Give the position of every leukocyte visible.
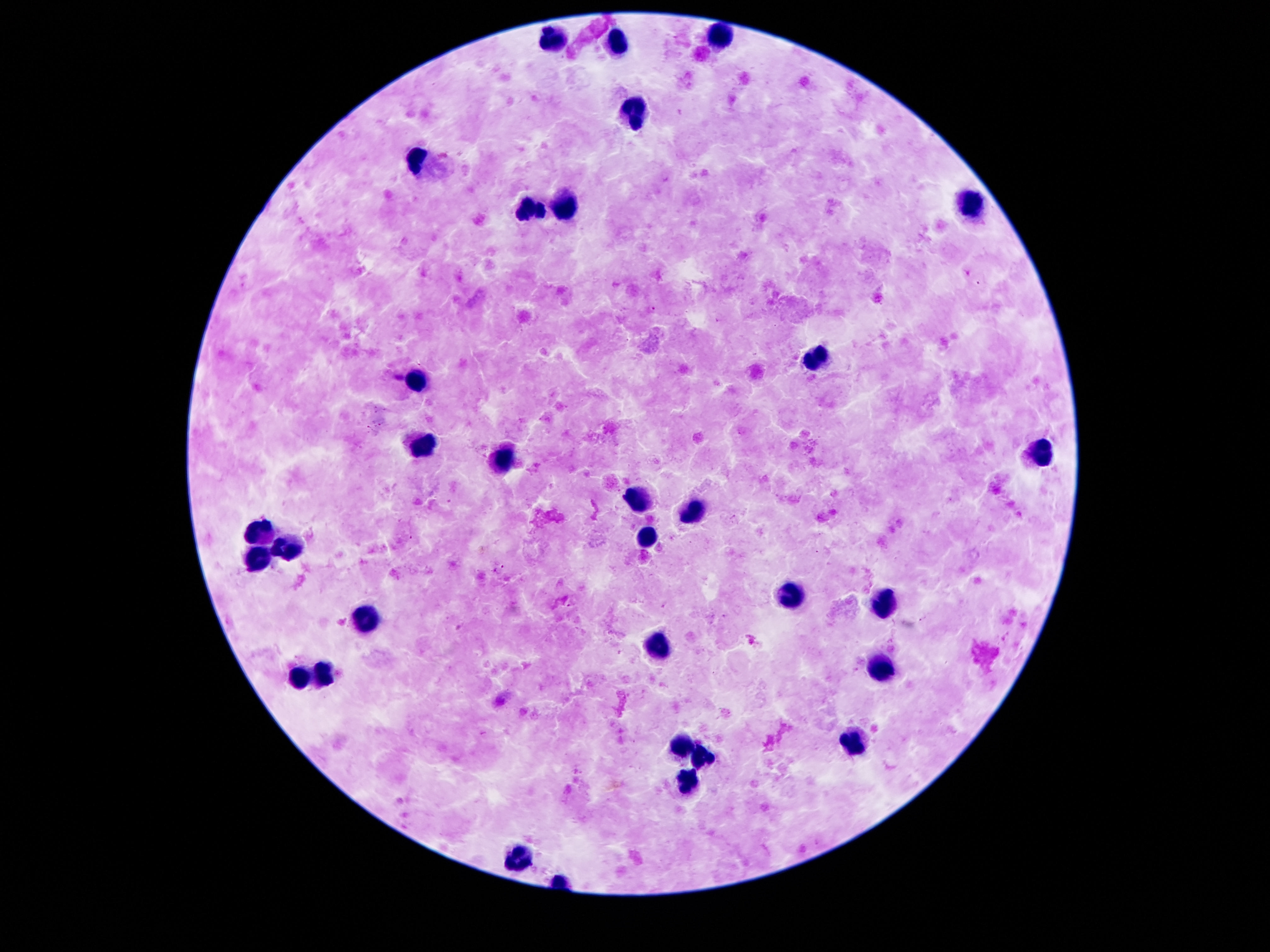
Approximate centers as {x, y} in pixels.
Leukocytes: {720, 35}, {550, 39}, {618, 43}, {632, 115}, {419, 158}, {972, 201}, {560, 203}, {529, 211}, {821, 356}, {419, 377}, {425, 447}, {1040, 453}, {503, 459}, {638, 496}, {698, 512}, {263, 531}, {646, 537}, {292, 549}, {257, 559}, {790, 592}, {886, 602}, {368, 615}, {657, 645}, {882, 666}, {327, 672}, {298, 678}, {853, 740}, {681, 744}, {704, 760}, {681, 781}, {515, 854}.

Summary:
  - Preparation: thick peripheral-blood smear
  - Magnification: 100x
  - Field of view: single
  - Image size: 1270×952 pixels
  - Capture: smartphone camera through the microscope eyepiece
  - Patient malaria status: uninfected
  - Stain: Giemsa